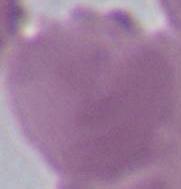
magnification: 1000x
identification: erythrocyte
modality: photomicrograph